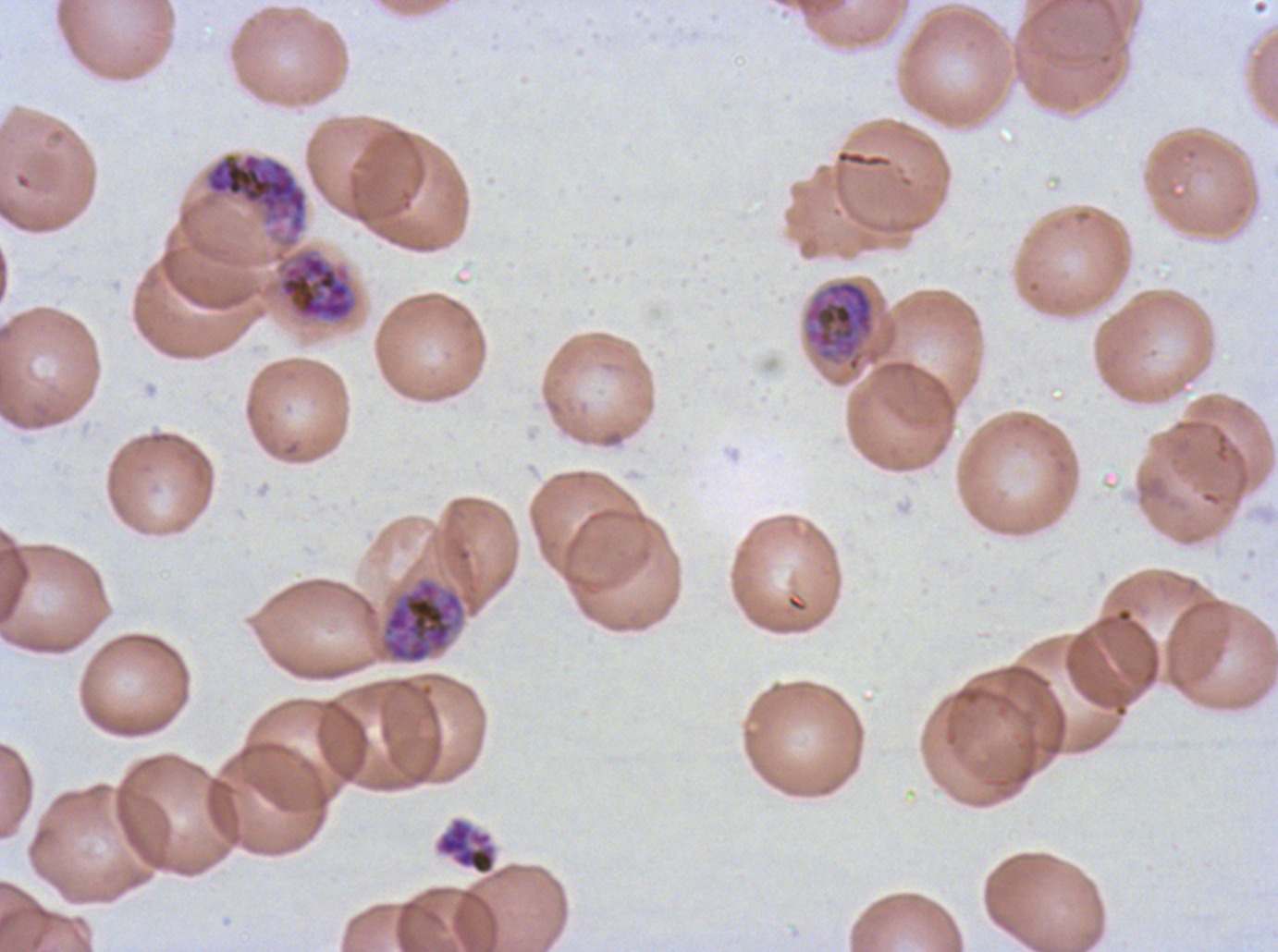

Approximate bounding rectangles given as corner coordinates in pixels from the top-left.
Summary:
  - Late schizont locations: (x1=202, y1=151, x2=309, y2=250), (x1=277, y1=250, x2=357, y2=323), (x1=382, y1=579, x2=465, y2=664), (x1=435, y1=817, x2=497, y2=875)
  - Early schizont locations: (x1=803, y1=279, x2=875, y2=372)
  - Specimen: P. falciparum cultured ex vivo for 24 to 48 hours, from a patient in The Gambia
  - Preparation: thin blood smear
  - Field of view: one sub-image of a larger composite
  - Stain: Giemsa
  - Life-cycle stages observed: early schizont, late schizont
  - Image size: 1278×952 pixels